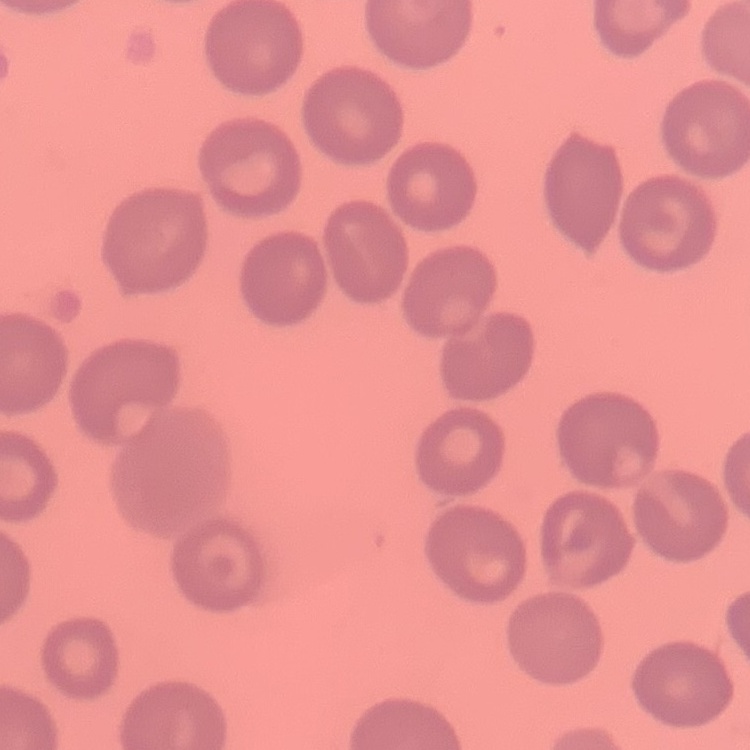
red blood cell morphology = no rouleaux formation
preparation = thin blood film
stain = Field's or Giemsa
image type = square crop of a larger photomicrograph